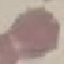

Result: no malaria parasites detected. Giemsa-stained preparation. Acquired by smartphone through the microscope eyepiece. Cell patch, automatically extracted from a larger field of view and resized to 64 × 64 pixels. Thin blood film.